Assess this cell for malaria.
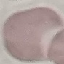

Uninfected.

capture = smartphone through the microscope eyepiece
preparation = thin blood film
stain = Giemsa
image type = cell patch, automatically extracted from a larger field of view and resized to 64 × 64 pixels